Name the parasite shown.
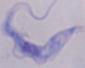

This is a trypanosome.

modality = micrograph
magnification = 1000x